Name the cell type shown.
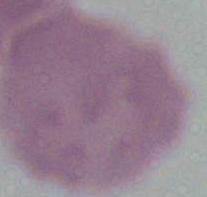
An erythrocyte.

Summary:
  - Modality: micrograph
  - Magnification: 1000x